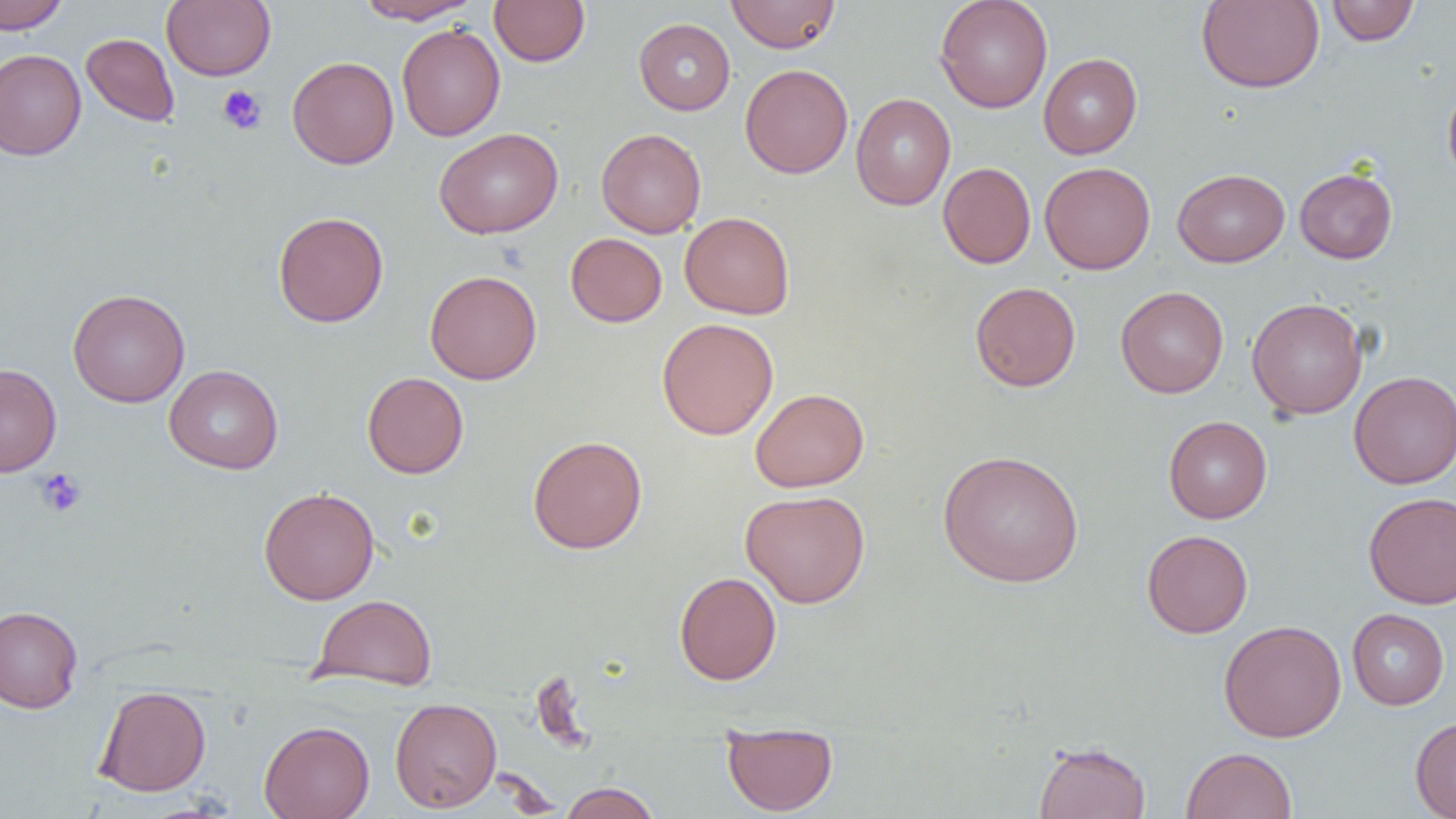
Approximate bounding boxes as (x1,y1)-(x2,y2) corner pairs in pixels. Platelet locations: (217,85)-(267,134), (35,467)-(87,517). Uninfected red blood cell locations: (0,0)-(69,33), (161,0)-(276,81), (354,0)-(482,24), (489,0)-(590,66), (725,0)-(841,53), (934,0)-(1053,113), (1196,1)-(1324,93), (1326,1)-(1419,46), (634,18)-(735,115), (397,24)-(505,141), (81,33)-(180,126), (0,49)-(86,161), (1038,53)-(1142,159), (287,56)-(399,169), (740,64)-(853,178), (1442,78)-(1456,186), (851,93)-(956,210), (434,127)-(563,239), (596,128)-(706,238), (1039,161)-(1156,274), (937,162)-(1036,269), (1294,167)-(1397,263), (1173,168)-(1290,267), (273,211)-(388,327), (680,211)-(795,319), (566,233)-(667,327), (425,270)-(542,385), (970,281)-(1081,392), (1115,286)-(1229,398), (67,288)-(190,407), (1246,298)-(1367,419), (656,318)-(779,439), (0,363)-(62,477), (164,365)-(284,474), (1348,370)-(1456,489), (362,372)-(469,478), (750,388)-(869,492), (1163,416)-(1273,523), (527,435)-(647,554), (937,449)-(1084,588), (258,486)-(379,605), (741,490)-(870,608), (1363,491)-(1456,608), (1141,529)-(1253,638), (674,571)-(781,685), (312,594)-(437,691), (0,606)-(83,713), (1347,608)-(1449,710), (1218,619)-(1346,743), (94,685)-(212,796), (390,697)-(502,813), (1410,716)-(1456,818), (259,720)-(375,819), (721,721)-(838,816), (1034,740)-(1151,819), (1182,747)-(1298,819), (560,782)-(661,819). Slide-level diagnosis: no evidence of blood parasites. Image is 1456×819 pixels. Thin blood film. Light microscopy. One field of a larger specimen. Captured at 1000x magnification.